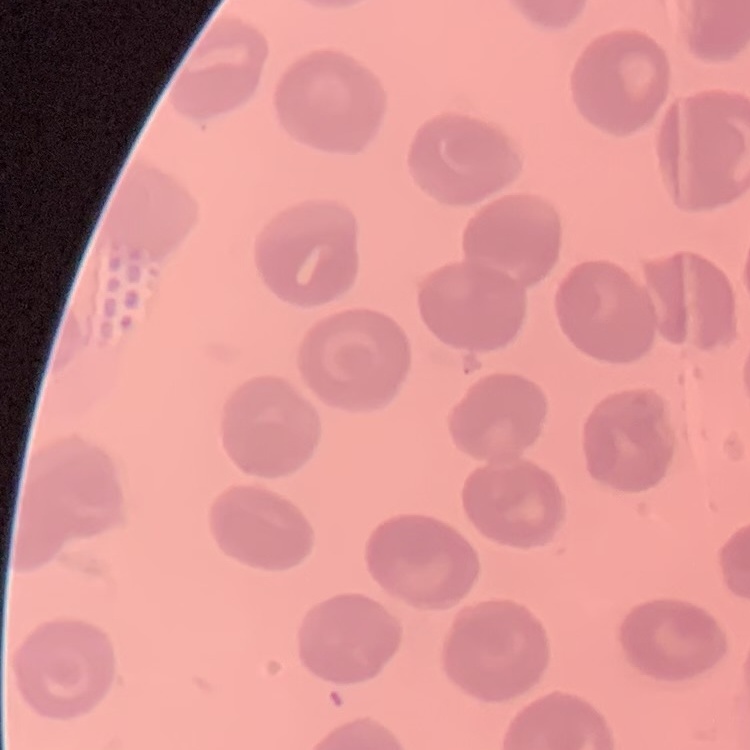
red blood cell morphology = no rouleaux formation
stain = Field's or Giemsa
preparation = thin blood smear
image type = one tile cut from a larger photomicrograph